Classify this cell by malaria status.
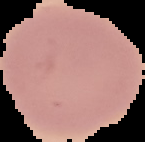
It is uninfected.

Cell region segmented out of the field of view; the surrounding area is masked to black. Image is 145×142 pixels. From a thin blood smear.